Assess the morphology of the erythrocytes.
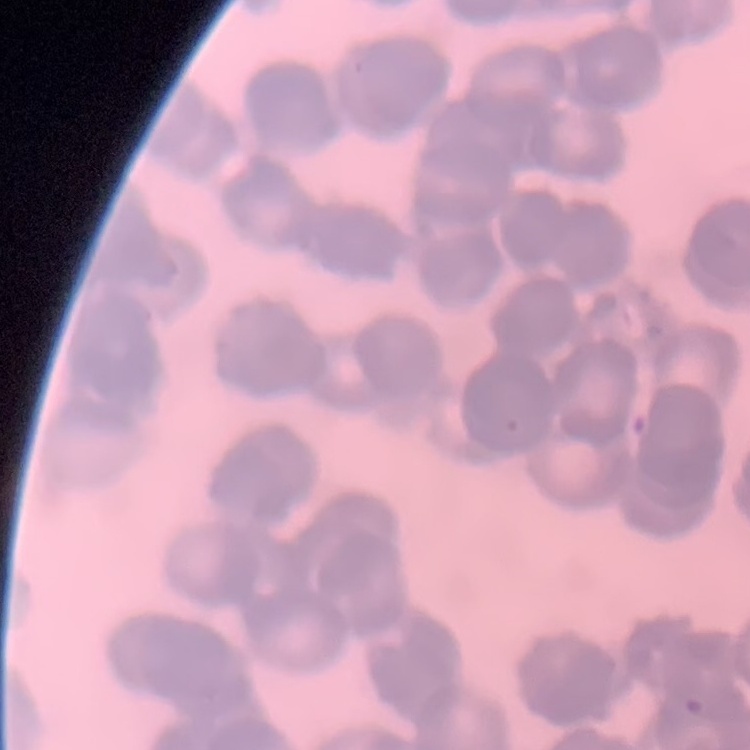

Rouleaux formation.

{
  "image_type": "square crop of a larger photomicrograph",
  "stain": "Field's or Giemsa",
  "preparation": "thin blood film"
}